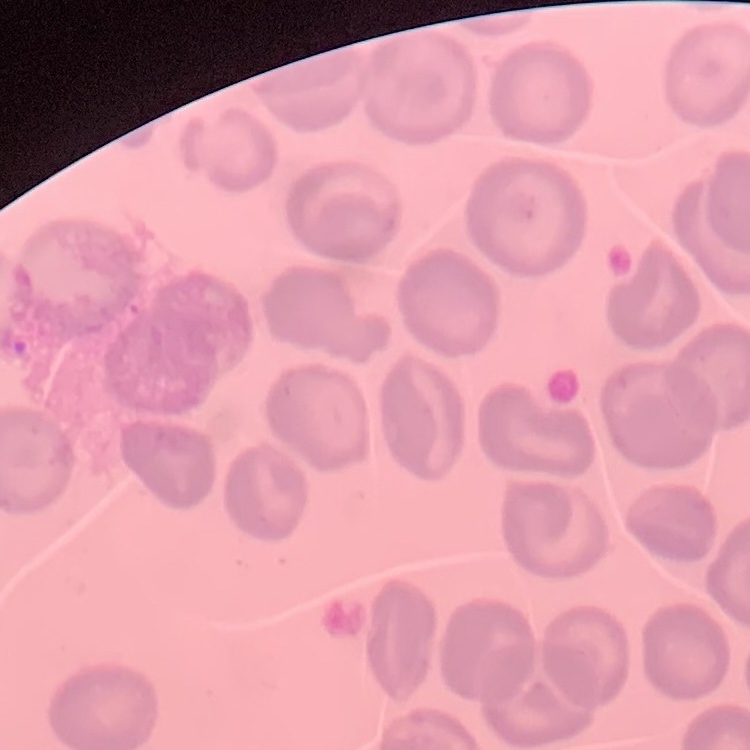

Summary:
  - Erythrocyte morphology: no rouleaux formation
  - Stain: Field's or Giemsa
  - Image type: square crop of a larger photomicrograph
  - Preparation: thin peripheral smear